Mark where platelets are.
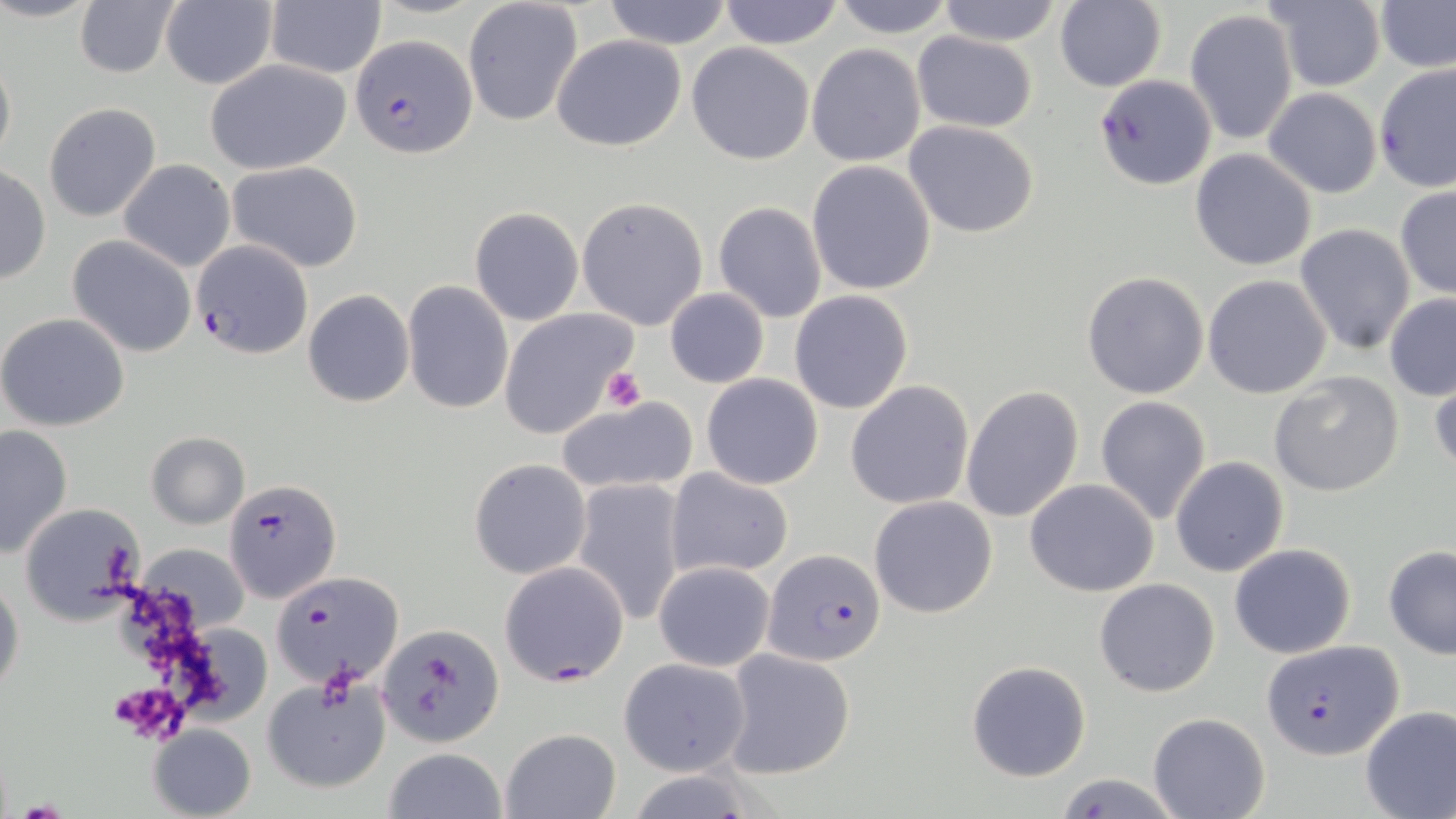
Approximate bounding boxes as (x1,y1)-(x2,y2) corner pairs in pixels.
Platelets: (602,367)-(645,413), (420,655)-(460,713), (108,685)-(186,738), (13,798)-(69,818).

Uninfected red blood cell locations: (161,0)-(279,89), (601,0)-(733,49), (718,0)-(845,48), (829,0)-(957,38), (935,0)-(1063,45), (1377,0)-(1455,73), (73,1)-(181,79), (265,1)-(387,80), (1053,1)-(1166,91), (1262,1)-(1387,90), (462,2)-(582,126), (1184,8)-(1299,146), (912,32)-(1038,131), (552,34)-(686,152), (685,42)-(815,165), (808,44)-(927,166), (0,48)-(16,171), (204,60)-(352,174), (1374,65)-(1456,193), (1094,75)-(1217,190), (1262,88)-(1381,197), (43,101)-(162,222), (903,120)-(1041,238), (1191,149)-(1317,271), (118,160)-(234,273), (226,160)-(364,272), (807,161)-(936,294), (0,164)-(51,286), (1394,185)-(1456,301), (577,197)-(708,331), (713,201)-(827,323), (470,206)-(582,325), (1294,224)-(1417,355), (67,236)-(198,358), (1082,272)-(1208,399), (1203,273)-(1333,399), (403,281)-(514,414), (664,288)-(768,387), (303,290)-(414,407), (789,291)-(913,414), (1384,293)-(1456,401), (501,308)-(638,438), (0,312)-(130,431), (1428,368)-(1456,479), (1268,371)-(1404,497), (701,374)-(823,490), (846,380)-(975,509), (961,384)-(1085,525), (553,395)-(702,498), (1094,396)-(1212,524), (0,423)-(73,559), (146,432)-(249,528), (1171,456)-(1289,577), (469,458)-(592,579), (666,467)-(794,578), (572,479)-(687,625), (1025,479)-(1159,597), (869,495)-(998,618), (17,501)-(145,626), (1229,542)-(1357,658), (138,544)-(252,631), (1382,544)-(1456,658), (653,560)-(774,671), (0,574)-(25,700), (1094,576)-(1221,698), (378,623)-(505,748), (722,648)-(855,779), (617,657)-(752,776), (965,659)-(1091,781), (261,676)-(394,796), (1359,705)-(1456,818), (1148,710)-(1271,819), (148,724)-(256,819), (501,728)-(621,819), (381,748)-(508,819), (1052,771)-(1183,818). Plasmodium falciparum-infected red blood cell locations: (353,34)-(477,157), (192,239)-(316,359), (224,478)-(341,604), (764,548)-(888,665), (499,561)-(630,685), (274,571)-(405,689), (1262,640)-(1402,762). Slide-level diagnosis: Plasmodium falciparum. Thin blood film. May-Grünwald-Giemsa-stained preparation. Image is 1456×819 pixels. Light microscopy. One field of a larger specimen. Captured at 1000x magnification.